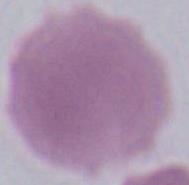

1000x magnification. A red blood cell is seen. Micrograph.